Locate every Plasmodium falciparum-infected red blood cell.
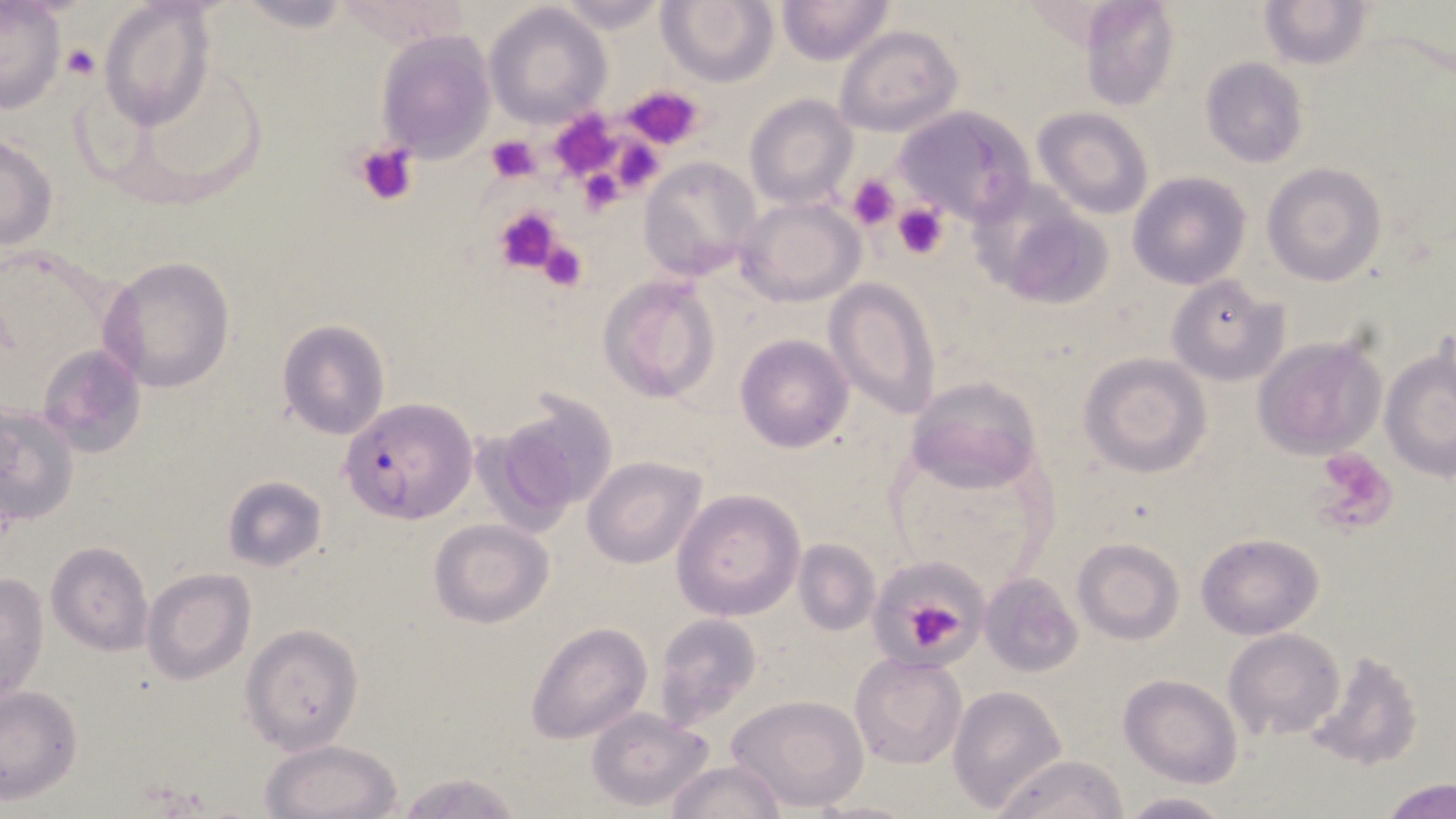

Approximate bounding boxes as (x1,y1)-(x2,y2) corner pairs in pixels.
Plasmodium falciparum-infected red blood cells: (341,397)-(478,524).

Summary:
  - Platelet locations: (60,42)-(100,80), (623,85)-(706,149), (486,134)-(541,182), (353,142)-(420,207), (847,173)-(900,233), (890,203)-(949,259), (492,204)-(563,276), (537,238)-(590,292), (1309,450)-(1399,536), (907,604)-(961,651)
  - Uninfected red blood cell locations: (655,0)-(779,88), (775,0)-(894,66), (1078,0)-(1181,111), (1257,0)-(1376,69), (100,2)-(216,133), (545,2)-(673,32), (0,3)-(66,116), (484,4)-(611,127), (834,24)-(963,137), (374,30)-(494,163), (1200,57)-(1309,168), (743,93)-(858,210), (892,106)-(1036,230), (1033,107)-(1154,220), (0,133)-(58,251), (638,156)-(763,280), (1261,163)-(1386,286), (1127,171)-(1251,291), (971,184)-(1110,310), (735,197)-(865,307), (99,255)-(236,393), (598,274)-(723,405), (1165,275)-(1284,386), (825,277)-(941,420), (277,320)-(390,440), (735,334)-(854,454), (1252,337)-(1385,459), (37,343)-(145,458), (1381,349)-(1456,479), (1078,352)-(1212,478), (904,377)-(1042,496), (484,390)-(620,527), (0,403)-(80,525), (581,456)-(708,568), (221,475)-(329,573), (670,487)-(806,622), (430,520)-(554,629), (1196,533)-(1323,639), (792,537)-(881,637), (1073,538)-(1185,644), (46,542)-(152,656), (141,569)-(256,684), (0,573)-(49,709), (980,573)-(1081,676), (652,614)-(763,729), (525,621)-(654,745), (240,623)-(363,754), (1223,630)-(1345,742), (1303,648)-(1424,771), (849,651)-(966,771), (1120,674)-(1241,788), (948,686)-(1066,811), (0,687)-(83,802), (727,694)-(869,812), (585,706)-(717,810), (259,738)-(403,819), (991,754)-(1130,819), (664,759)-(787,819), (390,772)-(528,819), (1380,777)-(1454,819), (1115,791)-(1233,818), (808,799)-(922,819)
  - Slide-level diagnosis: Plasmodium falciparum
  - Magnification: 1000x
  - Modality: light microscopy
  - Image size: 1456×819 pixels
  - Preparation: thin blood film
  - Stain: May-Grünwald-Giemsa
  - Field of view: single